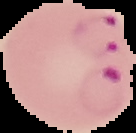
Cell region segmented out of the field of view; the surrounding area is masked to black. From a thin blood smear. Image is 136×133 pixels. Malaria status: parasitized.